Identify the parasite.
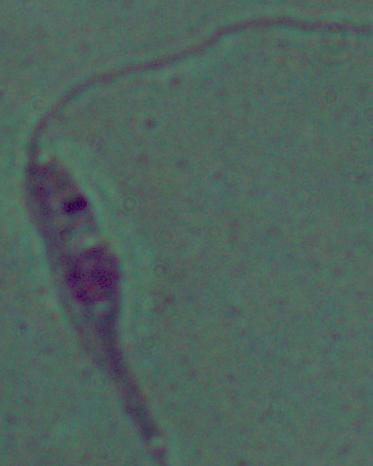

This is Leishmania.

Summary:
  - Magnification: 1000x
  - Modality: micrograph